Point out each Plasmodium parasite.
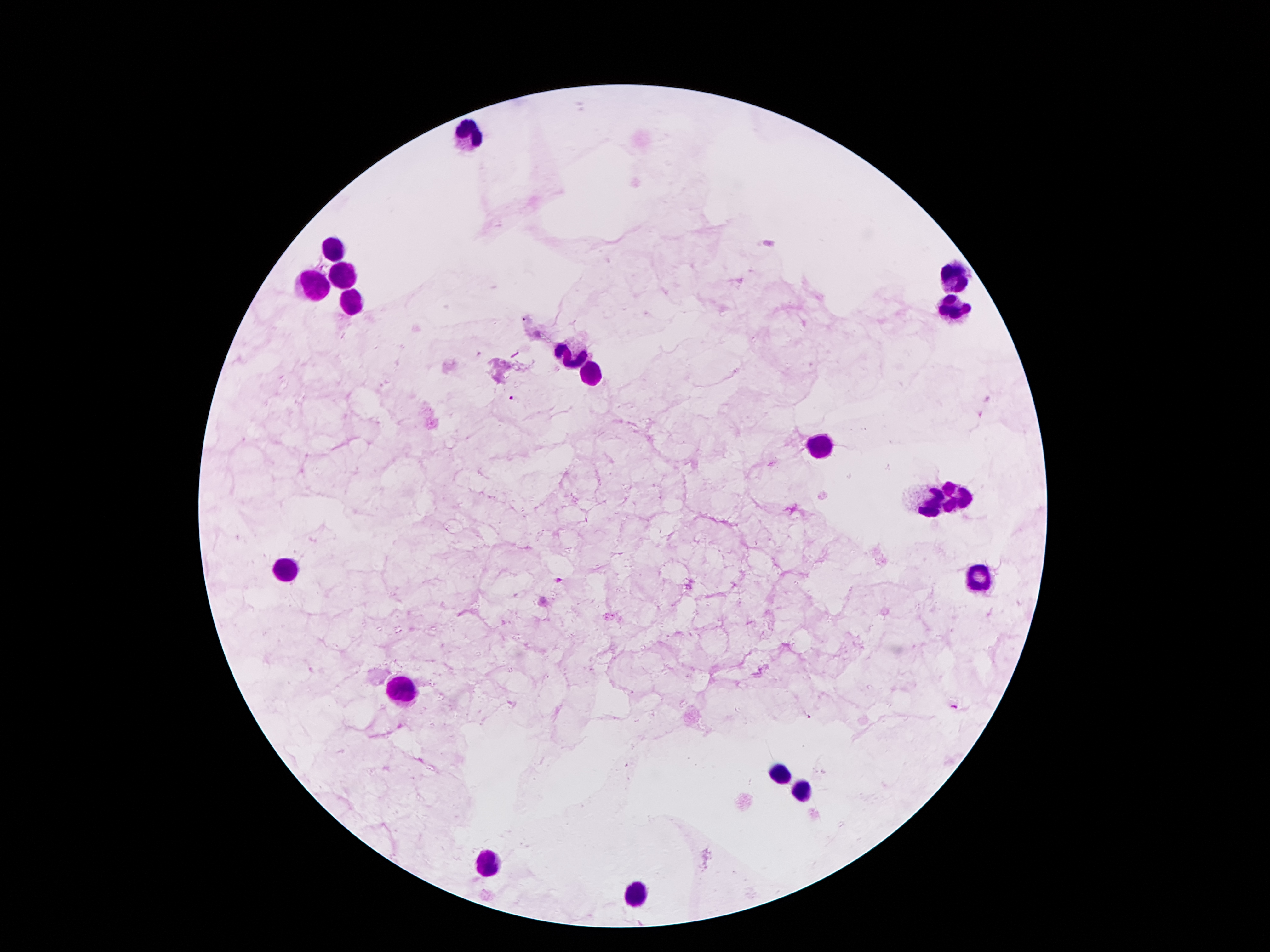
Approximate centers as (x, y) in pixels.
Plasmodium parasites: (514, 400), (559, 580), (806, 716).

{
  "field_of_view": "one from this slide",
  "patient_malaria_status": "positive for Plasmodium falciparum",
  "image_size": "1270×952 pixels",
  "stain": "Giemsa",
  "magnification": "100x",
  "leukocyte_locations": "approximate centers as (x, y) in pixels: (468, 137), (332, 245), (344, 277), (952, 277), (312, 282), (349, 302), (952, 312), (569, 357), (591, 379), (821, 443), (955, 497), (930, 502), (287, 566), (972, 581), (401, 685), (783, 774), (802, 791), (486, 863), (639, 893)",
  "preparation": "thick blood smear",
  "capture": "smartphone camera through the microscope eyepiece"
}